Locate every leukocyte (white blood cell).
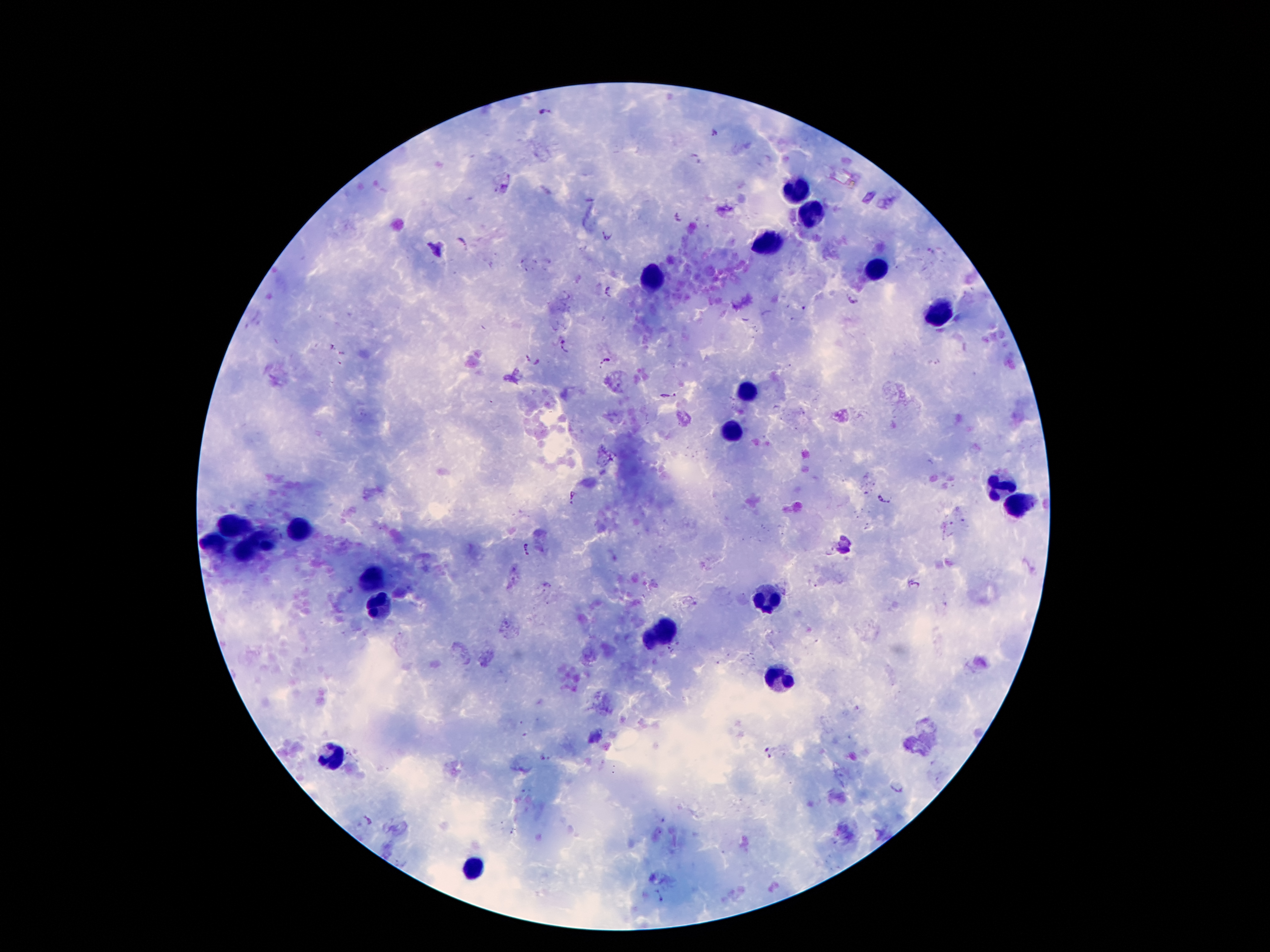

Approximate centers as {x, y} in pixels.
Leukocytes: {794, 191}, {808, 213}, {769, 242}, {878, 272}, {652, 279}, {943, 313}, {743, 391}, {734, 430}, {1001, 485}, {1019, 504}, {232, 525}, {302, 533}, {263, 539}, {213, 546}, {240, 553}, {374, 578}, {765, 598}, {380, 613}, {663, 633}, {777, 678}, {335, 756}, {470, 870}.

Plasmodium parasite locations: {544, 111}, {714, 134}, {695, 159}, {678, 218}, {608, 232}, {463, 242}, {607, 290}, {852, 299}, {567, 348}, {527, 356}, {607, 359}, {539, 361}, {670, 395}, {573, 497}, {885, 497}, {526, 550}, {766, 753}, {546, 756}, {899, 787}, {367, 821}, {662, 894}. Thick blood film. Patient malaria status: infected with Plasmodium falciparum. Giemsa stain. Photographed through the microscope eyepiece with a smartphone camera. One field from this slide. 100x magnification. Image is 1270×952 pixels.